Report the malaria status of this cell.
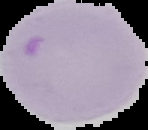
Uninfected.

Summary:
  - Image size: 148×130 pixels
  - Preparation: thin blood smear
  - Image type: cell region segmented out of the field of view; surrounding area masked to black